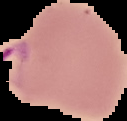

image type = cell region segmented out of the field of view; surrounding area masked to black
image size = 127×121 pixels
malaria status = parasitized
preparation = thin blood smear